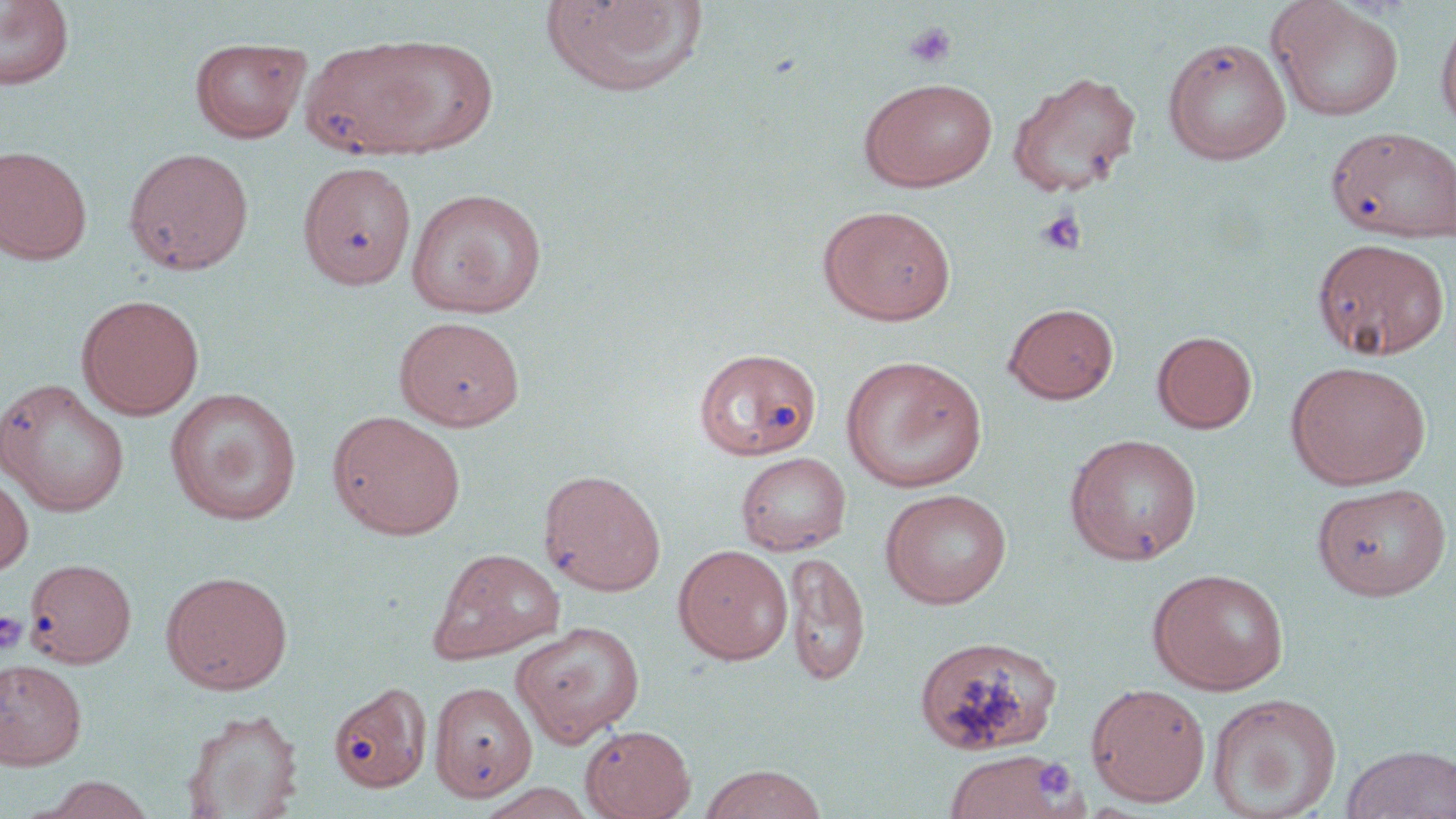
slide-level diagnosis = no evidence of blood parasites
magnification = 1000x
stain = May-Grünwald-Giemsa
image size = 1456×819 pixels
platelet locations = approximate bounding boxes as (x1,y1)-(x2,y2) corner pairs in pixels: (903,21)-(956,70), (1035,207)-(1086,256), (0,610)-(27,654), (1033,759)-(1076,801)
preparation = thin blood smear
field of view = one of a larger specimen
modality = optical microscopy
uninfected red blood cell locations = approximate bounding boxes as (x1,y1)-(x2,y2) corner pairs in pixels: (541,0)-(708,99), (1265,0)-(1405,123), (0,1)-(75,91), (1435,7)-(1456,134), (363,34)-(500,156), (189,36)-(310,143), (1163,37)-(1291,165), (301,39)-(445,160), (1006,70)-(1142,197), (858,77)-(998,192), (1326,126)-(1456,243), (0,146)-(91,265), (123,147)-(254,275), (298,161)-(416,290), (405,188)-(548,319), (818,205)-(956,325), (1312,238)-(1449,360), (76,294)-(205,419), (1003,302)-(1118,403), (394,316)-(526,430), (1153,330)-(1257,433), (694,348)-(821,461), (840,355)-(988,494), (1285,361)-(1431,490), (0,379)-(130,516), (165,388)-(302,525), (328,410)-(467,540), (1064,433)-(1202,565), (736,452)-(851,556), (539,468)-(666,596), (0,471)-(33,577), (1311,482)-(1453,600), (880,488)-(1012,609), (673,544)-(794,664), (426,548)-(566,665), (784,550)-(870,687), (24,558)-(136,667), (1147,568)-(1289,695), (160,570)-(293,694), (511,621)-(645,746), (914,635)-(1062,757), (0,658)-(87,770), (429,680)-(537,801), (1086,682)-(1211,806), (329,686)-(433,799), (1207,693)-(1342,818), (182,708)-(303,818), (580,723)-(696,819), (1341,743)-(1456,819), (943,750)-(1072,819), (699,764)-(828,819), (35,774)-(160,818), (477,782)-(599,818)